Report the malaria status of this cell.
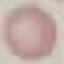
It is uninfected.

{
  "image_type": "cell patch, automatically extracted from a larger field of view and resized to 64 × 64 pixels",
  "preparation": "thin blood film",
  "stain": "Giemsa",
  "capture": "smartphone camera at the microscope eyepiece"
}